Name the parasite shown.
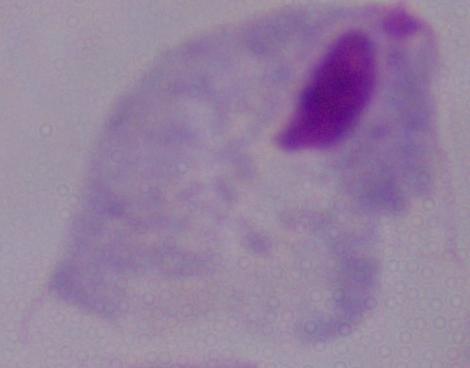
This is a trichomonad.

magnification = 1000x
modality = photomicrograph